Give the preparation type.
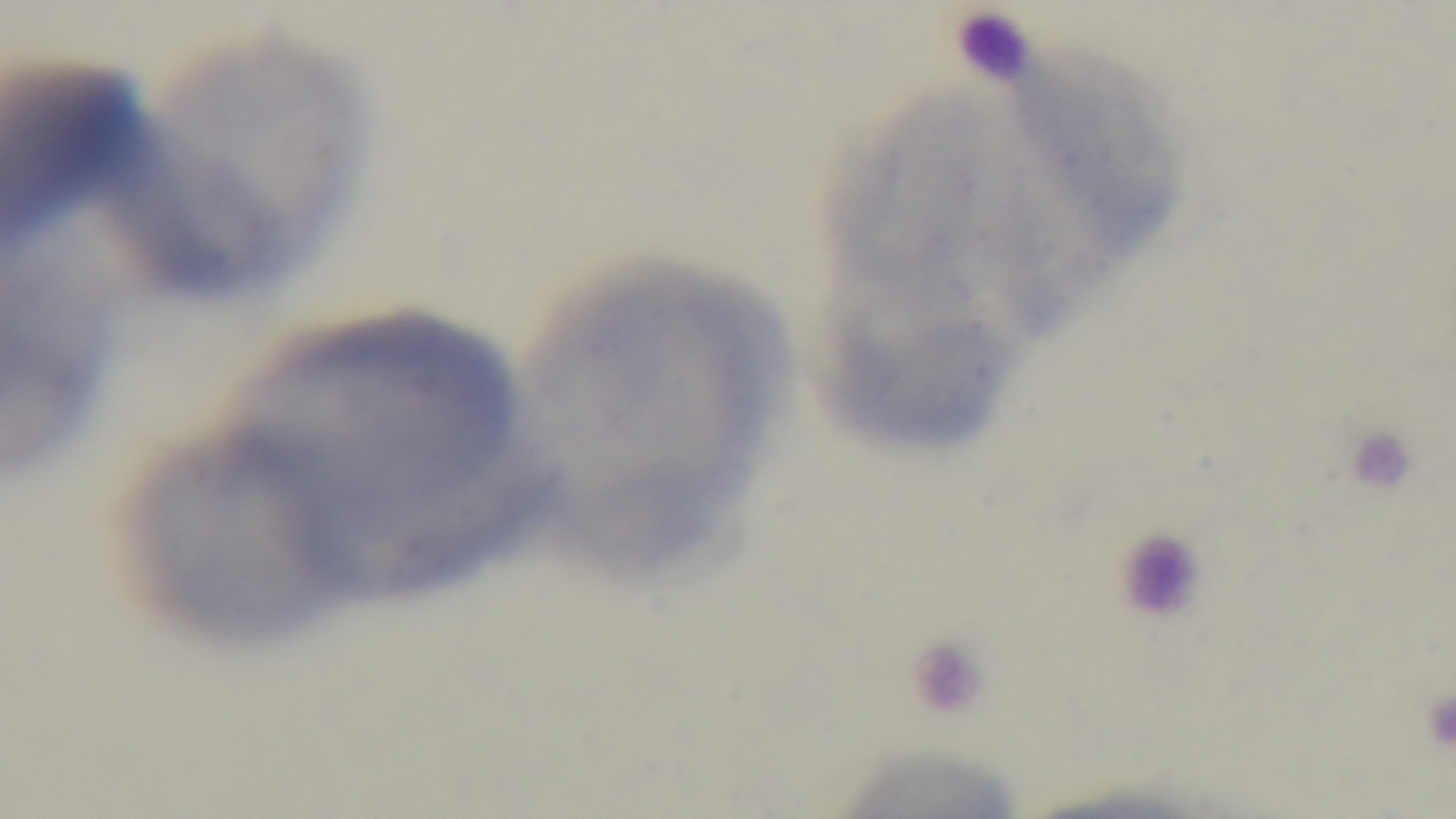

It is a thin blood film.

Summary:
  - Malaria status: uninfected
  - Objective: 100x oil immersion
  - Field of view: single
  - Stain: Giemsa
  - Modality: light microscopy
  - Capture: mounted 4K digital camera